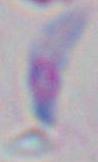

Summary:
  - Magnification: 1000x
  - Modality: photomicrograph
  - Identification: Toxoplasma gondii